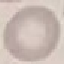

Result: no malaria parasites seen. Giemsa-stained preparation. Thin blood film. Acquired by smartphone through the microscope eyepiece. Cell patch, automatically extracted from a larger field of view and resized to 64 × 64 pixels.